Give the extent of all Plasmodium falciparum-infected red blood cells.
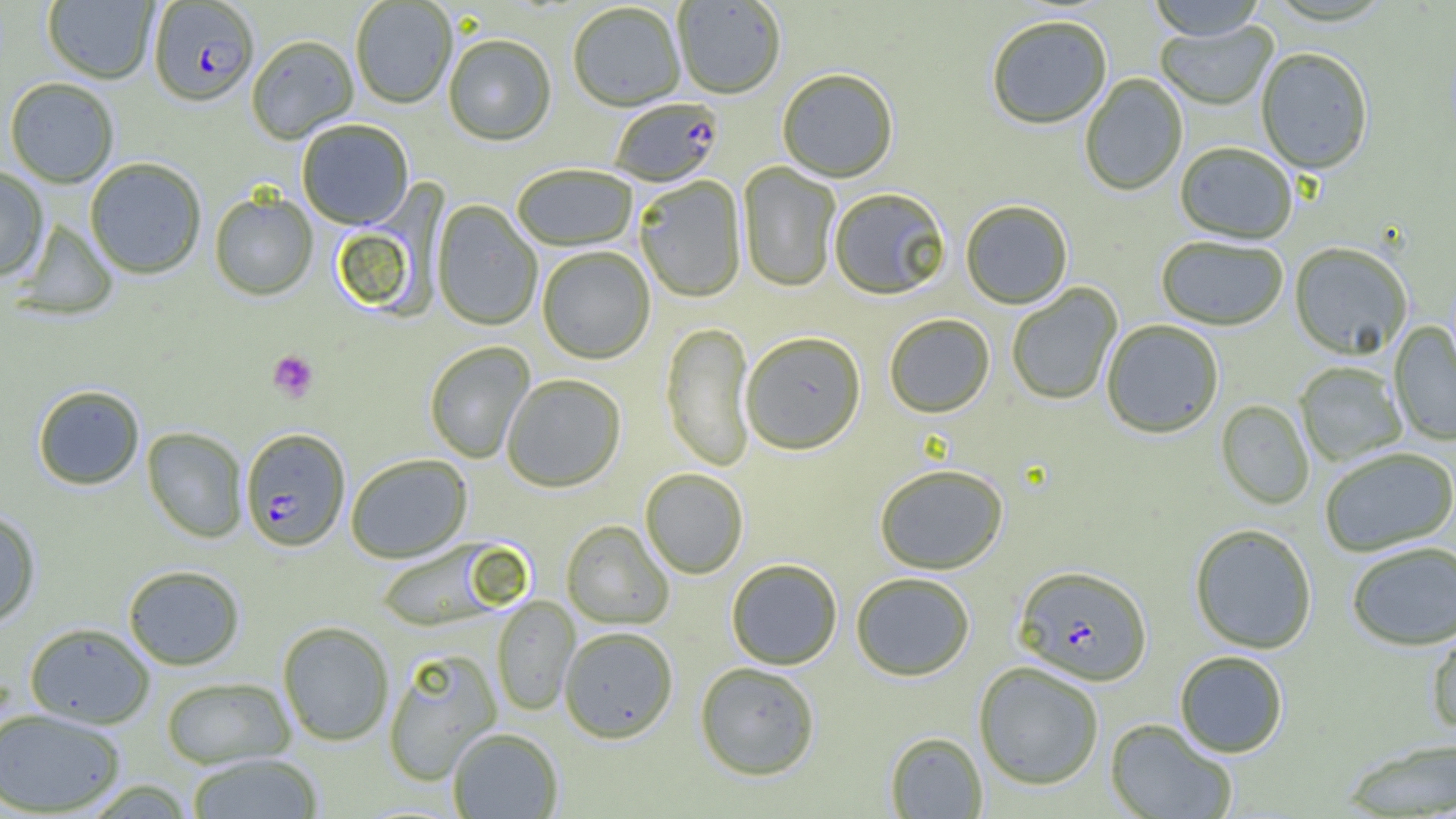

Approximate bounding boxes as (x1,y1)-(x2,y2) corner pairs in pixels.
Plasmodium falciparum-infected red blood cells: (148,2)-(259,109), (609,100)-(724,188), (241,428)-(350,552), (1014,566)-(1152,687).

{
  "slide_level_diagnosis": "Plasmodium falciparum",
  "platelet_locations": "approximate bounding boxes as (x1,y1)-(x2,y2) corner pairs in pixels: (268,349)-(319,402)",
  "magnification": "1000x",
  "image_size": "1456×819 pixels",
  "uninfected_red_blood_cell_locations": "approximate bounding boxes as (x1,y1)-(x2,y2) corner pairs in pixels: (42,0)-(158,85), (1146,0)-(1269,42), (351,1)-(457,109), (673,1)-(786,101), (568,4)-(685,113), (987,18)-(1112,131), (1155,21)-(1278,112), (247,37)-(358,145), (444,37)-(556,147), (1256,49)-(1372,176), (777,71)-(898,184), (1080,74)-(1188,197), (5,77)-(119,188), (297,120)-(413,230), (1175,144)-(1297,246), (85,158)-(206,279), (737,162)-(841,293), (512,166)-(638,252), (0,167)-(49,282), (635,176)-(747,304), (830,190)-(950,301), (210,191)-(318,301), (431,201)-(543,332), (960,202)-(1073,310), (13,219)-(119,320), (1157,237)-(1288,331), (1289,244)-(1412,360), (537,248)-(655,365), (1006,283)-(1123,406), (884,314)-(995,419), (1101,320)-(1223,439), (1389,321)-(1456,447), (660,322)-(755,472), (741,333)-(866,457), (424,341)-(536,464), (1294,362)-(1407,467), (501,374)-(626,493), (32,384)-(145,490), (1215,400)-(1314,510), (142,427)-(248,543), (1320,448)-(1456,557), (346,454)-(472,563), (874,465)-(1008,576), (640,469)-(749,579), (0,508)-(41,627), (561,520)-(674,630), (1189,524)-(1317,654), (375,539)-(515,631), (1347,542)-(1456,651), (726,559)-(842,670), (123,564)-(245,670), (851,573)-(975,682), (492,595)-(580,716), (277,621)-(394,746), (25,622)-(155,728), (1427,624)-(1456,737), (560,626)-(678,743), (383,649)-(502,786), (1174,651)-(1288,758), (974,662)-(1103,790), (695,663)-(820,781), (161,676)-(295,769), (0,707)-(126,817), (1105,719)-(1237,819), (447,728)-(563,819), (885,732)-(987,818), (1341,738)-(1456,817), (186,753)-(323,818)",
  "preparation": "thin blood film",
  "modality": "light microscopy",
  "field_of_view": "single"
}